Classify this cell by malaria status.
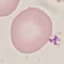

Uninfected.

stain: Giemsa
image_type: automatically extracted cell patch, resized to 64 × 64 pixels
preparation: thin blood smear
capture: smartphone through the microscope eyepiece